Evaluate for malaria.
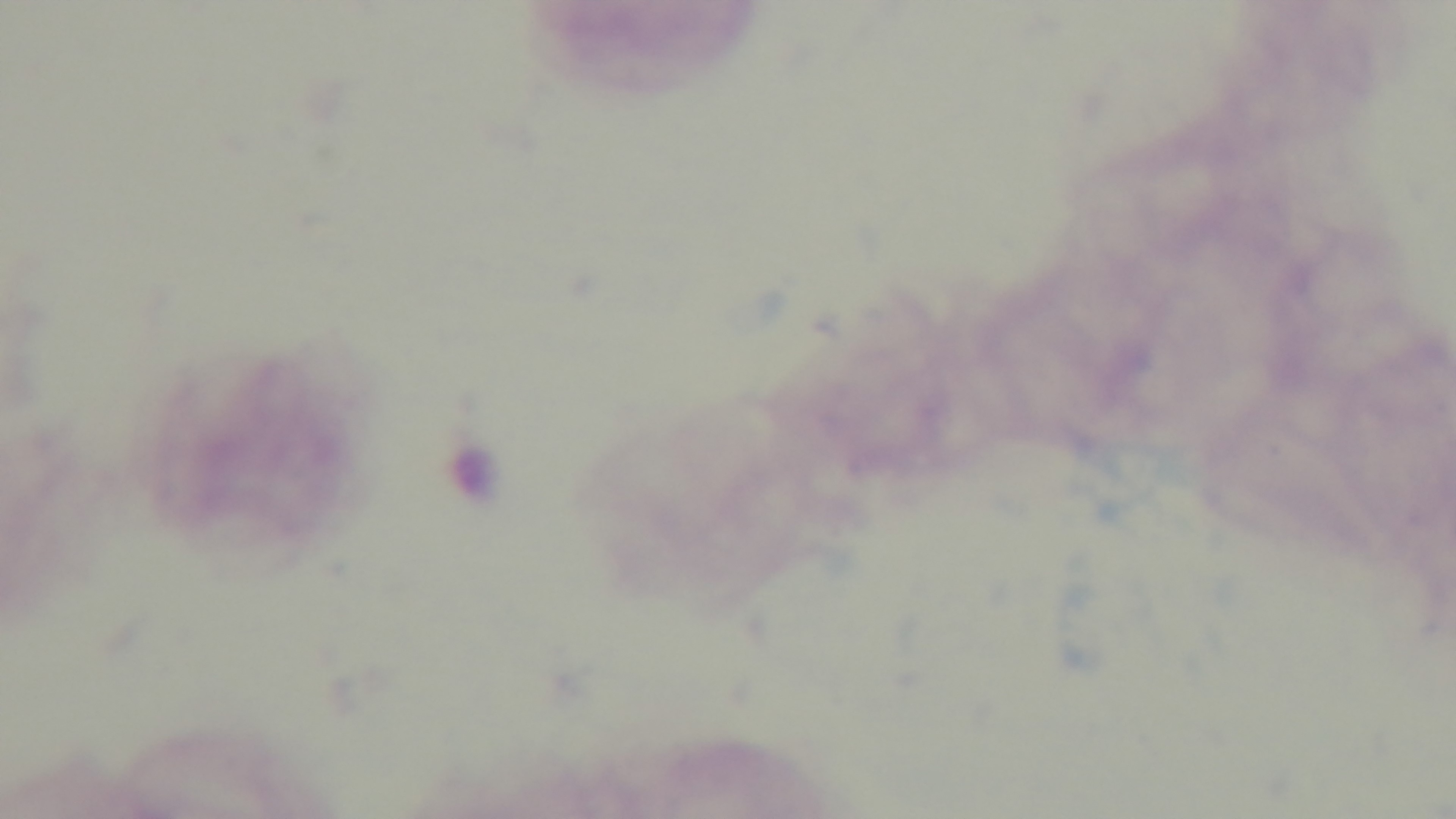

Uninfected.

Mounted 4K digital camera. Oil-immersion objective, 100x. Giemsa stain. One field from the slide. Preparation: thick smear. Light microscopy.